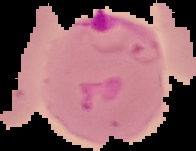
Summary:
  - Image size: 196×151 pixels
  - Result: malaria parasites detected
  - Image type: segmented cell region with the area outside set to black
  - Preparation: thin blood smear